Locate every blood parasite and identify its species.
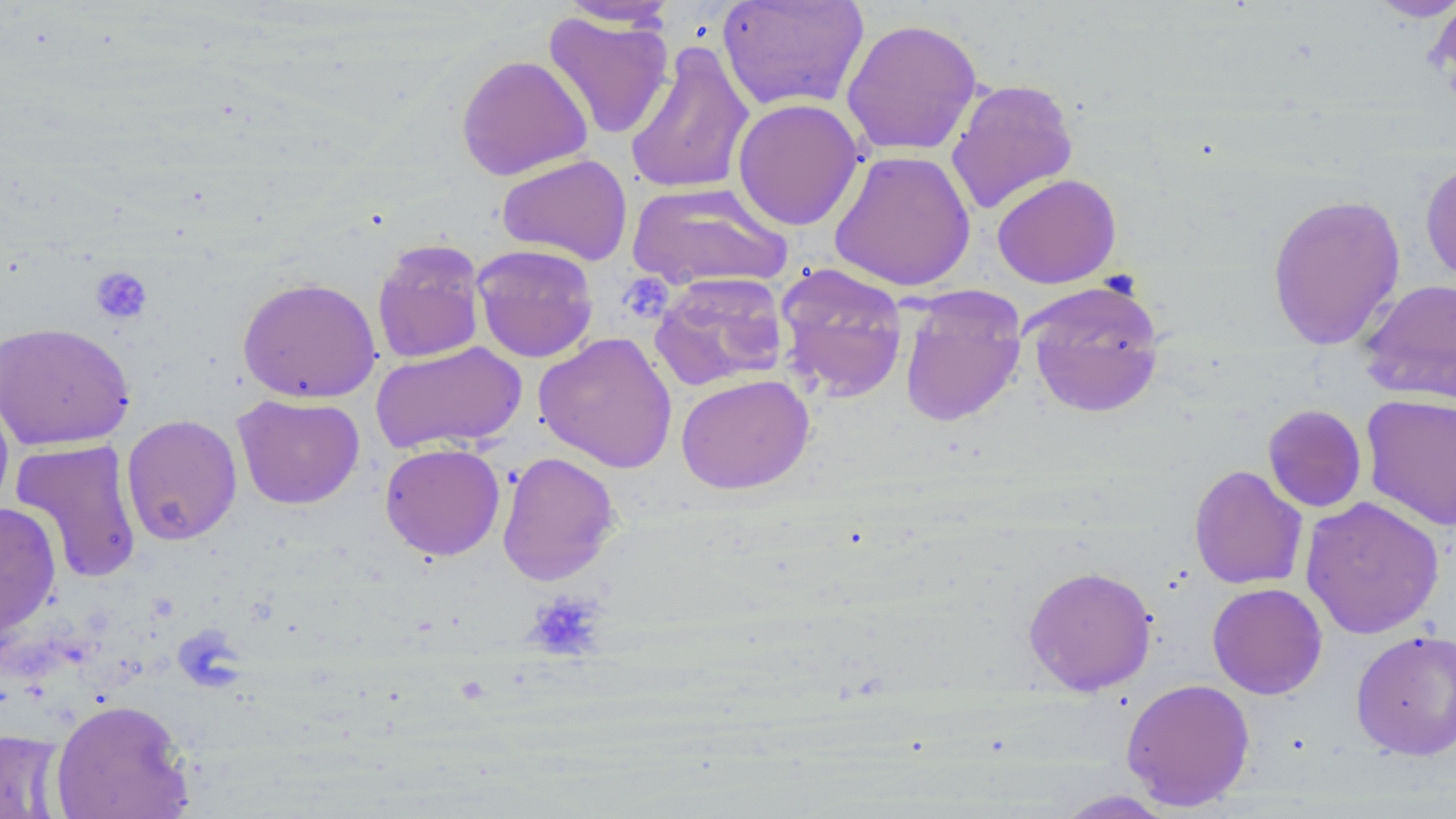

No blood parasites seen.

Approximate bounding boxes as [x1, y1, x2, y2] in pixels. Uninfected red blood cell locations: [717, 0, 870, 113], [1365, 0, 1455, 22], [1429, 0, 1456, 91], [557, 1, 678, 29], [542, 11, 674, 140], [840, 18, 983, 156], [624, 41, 755, 196], [456, 54, 593, 181], [945, 78, 1079, 215], [732, 98, 864, 231], [829, 149, 976, 291], [496, 154, 632, 266], [1420, 159, 1456, 286], [992, 173, 1122, 288], [627, 182, 793, 292], [1266, 193, 1406, 350], [371, 238, 487, 364], [471, 243, 599, 363], [775, 262, 909, 402], [649, 273, 789, 392], [237, 276, 381, 403], [1358, 277, 1456, 405], [1021, 280, 1166, 418], [898, 289, 1027, 427], [0, 321, 134, 451], [533, 332, 678, 473], [370, 341, 527, 455], [675, 374, 814, 495], [0, 385, 14, 521], [232, 393, 365, 509], [1361, 393, 1455, 531], [1262, 404, 1367, 512], [120, 414, 242, 545], [9, 439, 143, 584], [379, 442, 505, 561], [497, 451, 620, 586], [1188, 465, 1308, 590], [1300, 496, 1444, 639], [0, 502, 62, 641], [1023, 565, 1158, 695], [1207, 582, 1327, 699], [1351, 629, 1456, 761], [1121, 678, 1255, 811], [50, 698, 194, 819], [0, 728, 66, 819], [1054, 789, 1175, 818]. Platelet locations: [89, 266, 152, 325], [618, 275, 670, 317], [525, 591, 606, 660]. Slide-level diagnosis: no evidence of blood parasites. May-Grünwald-Giemsa stain. Image is 1456×819 pixels. 1000x magnification. Light microscopy. Thin blood smear. One field of a larger specimen.